Name the blood parasite species.
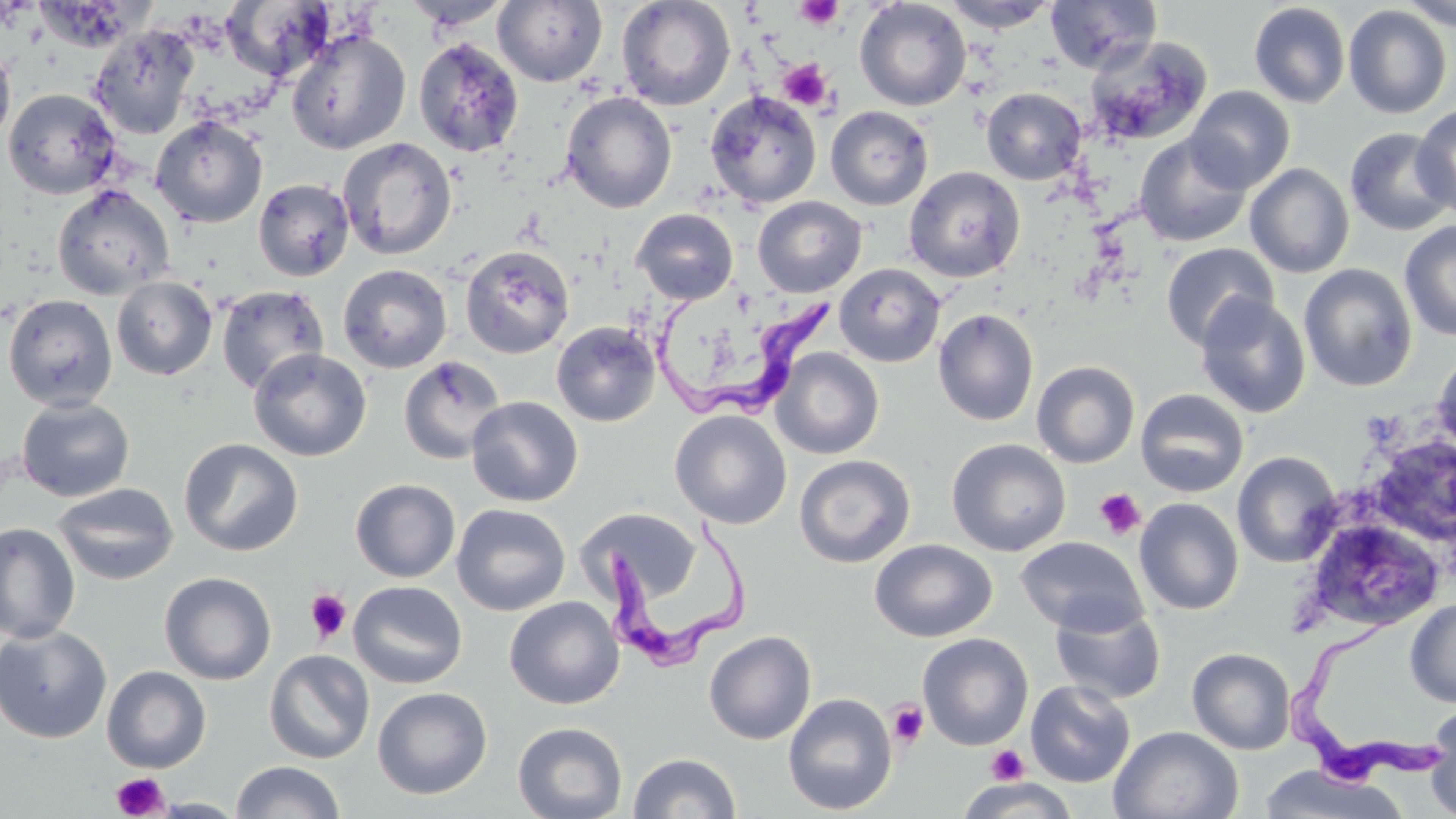
Trypanosoma brucei.

Approximate bounding boxes as named x1/y1/x2/y2 corners in pixels. Uninfected red blood cell locations: (x1=401, y1=0, x2=513, y2=30), (x1=493, y1=0, x2=608, y2=86), (x1=616, y1=0, x2=736, y2=111), (x1=854, y1=0, x2=972, y2=111), (x1=941, y1=0, x2=1059, y2=32), (x1=1045, y1=0, x2=1162, y2=75), (x1=1398, y1=0, x2=1456, y2=31), (x1=220, y1=2, x2=335, y2=79), (x1=1248, y1=2, x2=1351, y2=108), (x1=1343, y1=5, x2=1452, y2=119), (x1=88, y1=24, x2=200, y2=140), (x1=285, y1=29, x2=411, y2=155), (x1=1084, y1=36, x2=1212, y2=144), (x1=413, y1=38, x2=525, y2=158), (x1=0, y1=43, x2=16, y2=149), (x1=1186, y1=85, x2=1295, y2=193), (x1=981, y1=87, x2=1086, y2=185), (x1=2, y1=88, x2=122, y2=200), (x1=560, y1=91, x2=677, y2=213), (x1=704, y1=91, x2=821, y2=209), (x1=1412, y1=105, x2=1456, y2=220), (x1=825, y1=106, x2=933, y2=210), (x1=151, y1=116, x2=268, y2=228), (x1=1344, y1=127, x2=1456, y2=235), (x1=1134, y1=133, x2=1253, y2=247), (x1=337, y1=138, x2=457, y2=259), (x1=1244, y1=163, x2=1354, y2=278), (x1=904, y1=166, x2=1025, y2=283), (x1=253, y1=178, x2=355, y2=281), (x1=51, y1=184, x2=175, y2=300), (x1=752, y1=196, x2=867, y2=298), (x1=631, y1=208, x2=738, y2=304), (x1=1399, y1=220, x2=1456, y2=341), (x1=1160, y1=242, x2=1279, y2=350), (x1=460, y1=245, x2=574, y2=359), (x1=833, y1=263, x2=946, y2=367), (x1=1298, y1=263, x2=1417, y2=392), (x1=338, y1=264, x2=452, y2=373), (x1=111, y1=276, x2=217, y2=381), (x1=215, y1=285, x2=329, y2=396), (x1=2, y1=294, x2=118, y2=410), (x1=1195, y1=294, x2=1311, y2=419), (x1=933, y1=309, x2=1039, y2=426), (x1=552, y1=321, x2=660, y2=426), (x1=772, y1=347, x2=884, y2=459), (x1=1432, y1=347, x2=1456, y2=462), (x1=248, y1=348, x2=371, y2=462), (x1=398, y1=355, x2=506, y2=465), (x1=1032, y1=361, x2=1140, y2=468), (x1=1135, y1=388, x2=1249, y2=497), (x1=466, y1=396, x2=583, y2=506), (x1=16, y1=397, x2=135, y2=502), (x1=670, y1=410, x2=792, y2=529), (x1=179, y1=438, x2=303, y2=556), (x1=946, y1=438, x2=1070, y2=556), (x1=1366, y1=439, x2=1456, y2=546), (x1=1232, y1=451, x2=1342, y2=567), (x1=794, y1=454, x2=916, y2=568), (x1=350, y1=478, x2=461, y2=582), (x1=51, y1=482, x2=179, y2=586), (x1=1134, y1=498, x2=1244, y2=615), (x1=451, y1=503, x2=571, y2=616), (x1=568, y1=503, x2=700, y2=603), (x1=1315, y1=518, x2=1443, y2=628), (x1=0, y1=523, x2=80, y2=644), (x1=1015, y1=535, x2=1148, y2=636), (x1=869, y1=539, x2=997, y2=642), (x1=159, y1=572, x2=276, y2=685), (x1=348, y1=580, x2=467, y2=689), (x1=504, y1=596, x2=625, y2=709), (x1=1404, y1=598, x2=1456, y2=708), (x1=1049, y1=600, x2=1167, y2=704), (x1=0, y1=626, x2=112, y2=744), (x1=704, y1=630, x2=817, y2=745), (x1=918, y1=632, x2=1033, y2=750), (x1=1187, y1=647, x2=1296, y2=755), (x1=264, y1=649, x2=375, y2=764), (x1=102, y1=666, x2=211, y2=773), (x1=1025, y1=679, x2=1136, y2=787), (x1=372, y1=687, x2=492, y2=799), (x1=783, y1=692, x2=897, y2=815), (x1=1424, y1=700, x2=1456, y2=819), (x1=512, y1=721, x2=627, y2=818), (x1=1109, y1=725, x2=1244, y2=819), (x1=628, y1=752, x2=742, y2=818), (x1=230, y1=761, x2=346, y2=819), (x1=1254, y1=765, x2=1411, y2=819), (x1=954, y1=778, x2=1081, y2=818), (x1=150, y1=797, x2=247, y2=817). Platelet locations: (x1=795, y1=0, x2=844, y2=29), (x1=777, y1=58, x2=832, y2=110), (x1=1093, y1=487, x2=1146, y2=540), (x1=305, y1=588, x2=352, y2=643), (x1=886, y1=700, x2=930, y2=747), (x1=986, y1=745, x2=1029, y2=786), (x1=110, y1=772, x2=170, y2=818). Trypanosoma brucei locations: (x1=650, y1=299, x2=834, y2=418), (x1=606, y1=507, x2=756, y2=670), (x1=1287, y1=603, x2=1447, y2=789). Captured at 1000x magnification. Single field of view. Optical microscopy. May-Grünwald-Giemsa stain. Thin blood film. Image is 1456×819 pixels.